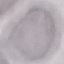

Malaria status: uninfected. Thin blood smear. Acquired by smartphone through the microscope eyepiece. Automatically extracted cell patch, resized to 64 × 64 pixels. Giemsa stain.